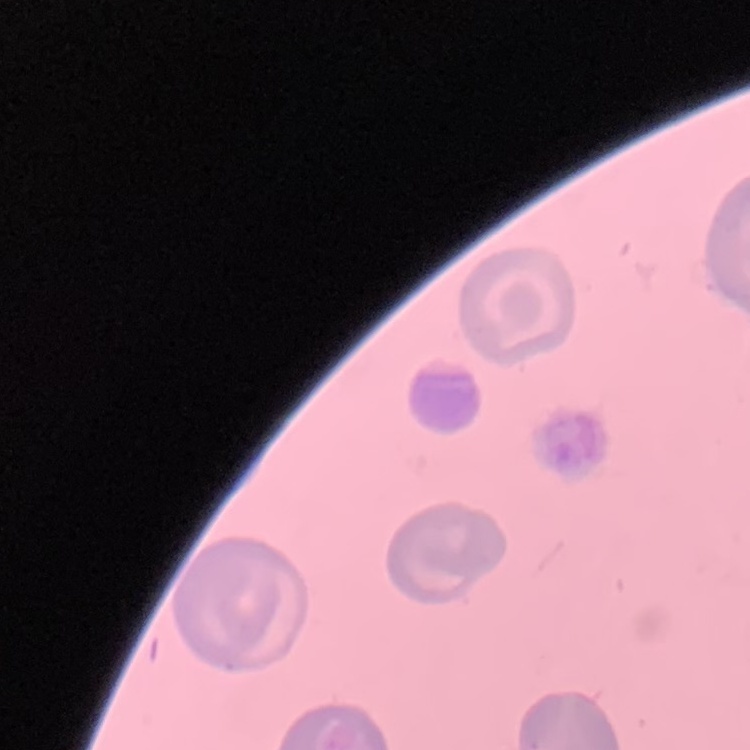

Summary:
  - Erythrocyte morphology: no rouleaux formation
  - Stain: Field's or Giemsa
  - Image type: one tile cut from a larger photomicrograph
  - Preparation: thin blood smear